Name the parasite shown.
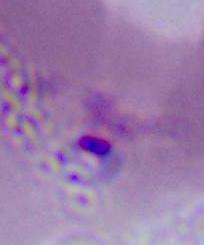
Plasmodium.

modality = micrograph
magnification = 400x or 1000x